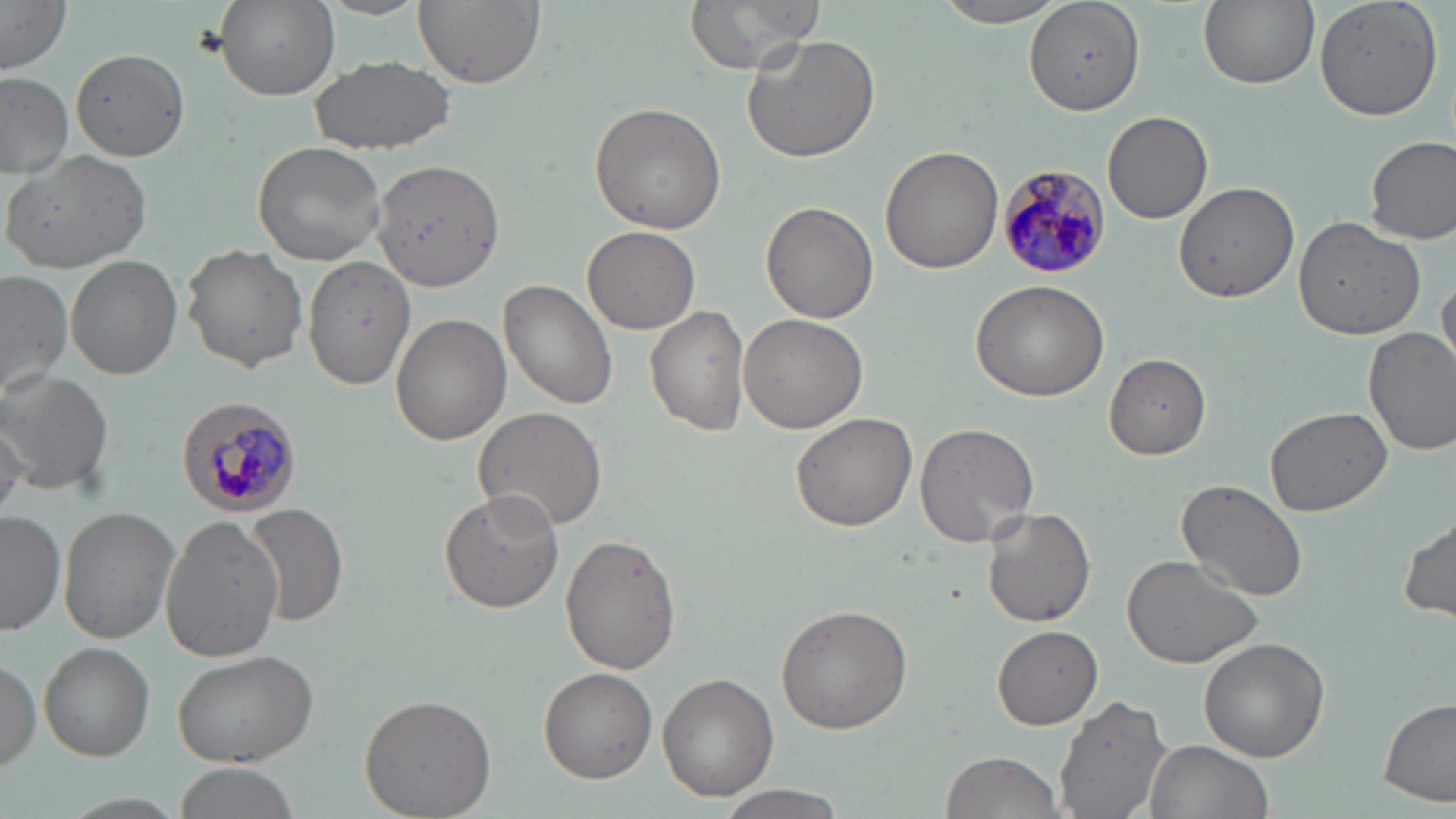
Summary:
  - Coordinate format: approximate bounding boxes as named x1/y1/x2/y2 corners in pixels
  - Plasmodium malariae-infected red blood cell locations: (x1=997, y1=164, x2=1113, y2=277), (x1=174, y1=397, x2=301, y2=518)
  - Uninfected red blood cell locations: (x1=217, y1=0, x2=340, y2=100), (x1=412, y1=0, x2=544, y2=89), (x1=684, y1=0, x2=828, y2=74), (x1=936, y1=0, x2=1068, y2=28), (x1=1026, y1=0, x2=1146, y2=117), (x1=1198, y1=0, x2=1319, y2=90), (x1=1315, y1=0, x2=1441, y2=121), (x1=0, y1=2, x2=71, y2=73), (x1=741, y1=30, x2=882, y2=163), (x1=70, y1=48, x2=189, y2=161), (x1=308, y1=54, x2=455, y2=156), (x1=0, y1=72, x2=73, y2=179), (x1=588, y1=101, x2=727, y2=234), (x1=1103, y1=110, x2=1213, y2=223), (x1=1367, y1=135, x2=1455, y2=245), (x1=253, y1=140, x2=386, y2=264), (x1=880, y1=144, x2=1004, y2=274), (x1=6, y1=149, x2=152, y2=276), (x1=369, y1=158, x2=504, y2=292), (x1=1173, y1=178, x2=1299, y2=301), (x1=760, y1=202, x2=878, y2=323), (x1=1293, y1=215, x2=1427, y2=339), (x1=583, y1=225, x2=701, y2=334), (x1=182, y1=245, x2=308, y2=370), (x1=303, y1=255, x2=415, y2=391), (x1=0, y1=270, x2=73, y2=395), (x1=1437, y1=274, x2=1456, y2=373), (x1=501, y1=279, x2=617, y2=410), (x1=969, y1=279, x2=1111, y2=402), (x1=645, y1=306, x2=751, y2=437), (x1=391, y1=313, x2=509, y2=444), (x1=736, y1=314, x2=870, y2=434), (x1=1363, y1=327, x2=1456, y2=453), (x1=1104, y1=354, x2=1213, y2=459), (x1=0, y1=367, x2=115, y2=495), (x1=1266, y1=405, x2=1391, y2=516), (x1=473, y1=406, x2=608, y2=533), (x1=792, y1=413, x2=917, y2=532), (x1=914, y1=420, x2=1040, y2=548), (x1=1, y1=421, x2=29, y2=521), (x1=1176, y1=479, x2=1310, y2=603), (x1=440, y1=489, x2=564, y2=611), (x1=249, y1=504, x2=349, y2=626), (x1=58, y1=505, x2=180, y2=644), (x1=982, y1=506, x2=1096, y2=627), (x1=0, y1=510, x2=64, y2=634), (x1=1399, y1=512, x2=1455, y2=624), (x1=160, y1=514, x2=284, y2=660), (x1=559, y1=534, x2=681, y2=673), (x1=1121, y1=551, x2=1267, y2=669), (x1=776, y1=603, x2=912, y2=734), (x1=992, y1=626, x2=1103, y2=727), (x1=1200, y1=637, x2=1329, y2=761), (x1=41, y1=642, x2=155, y2=760), (x1=170, y1=646, x2=321, y2=766), (x1=0, y1=654, x2=42, y2=775), (x1=538, y1=667, x2=655, y2=784), (x1=659, y1=673, x2=778, y2=801), (x1=358, y1=692, x2=496, y2=818), (x1=1056, y1=693, x2=1173, y2=819), (x1=1380, y1=695, x2=1455, y2=806), (x1=1143, y1=740, x2=1272, y2=819), (x1=940, y1=751, x2=1064, y2=819), (x1=171, y1=763, x2=301, y2=819), (x1=715, y1=785, x2=851, y2=817)
  - Slide-level diagnosis: Plasmodium malariae
  - Image size: 1456×819 pixels
  - Modality: light microscopy
  - Stain: May-Grünwald-Giemsa
  - Magnification: 1000x
  - Field of view: one of a larger specimen
  - Preparation: thin blood smear